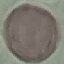

malaria status = uninfected
image type = automatically extracted cell patch, resized to 64 × 64 pixels
capture = smartphone camera at the microscope eyepiece
stain = Giemsa
preparation = thin blood smear